State the blood parasite species.
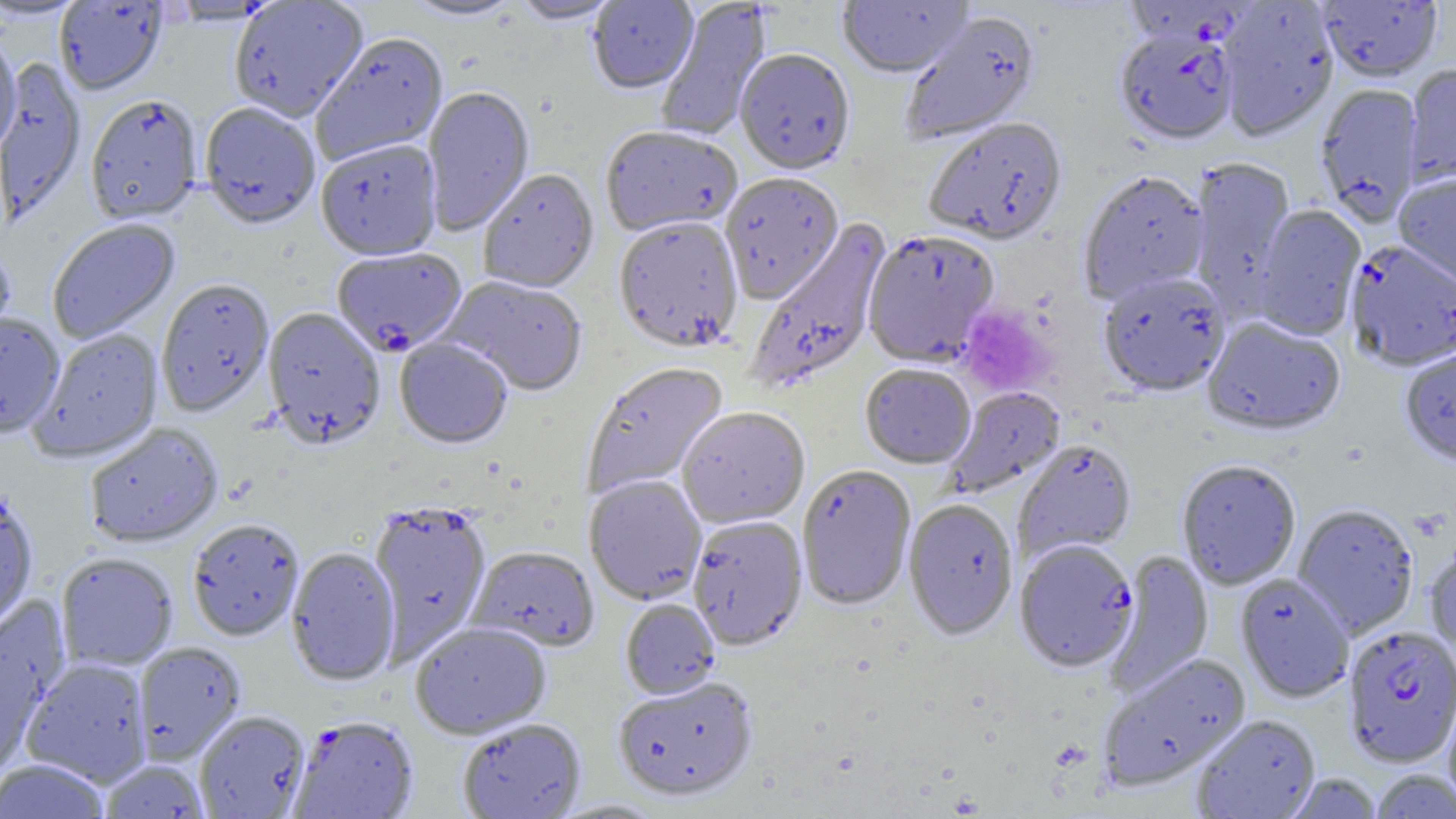

Plasmodium falciparum.

Summary:
  - Coordinate format: approximate bounding boxes as named x1/y1/x2/y2 corners in pixels
  - Platelet locations: (x1=957, y1=304, x2=1052, y2=396)
  - Plasmodium falciparum-infected red blood cell locations: (x1=1114, y1=30, x2=1237, y2=148), (x1=1345, y1=241, x2=1456, y2=373), (x1=332, y1=249, x2=467, y2=358), (x1=1015, y1=541, x2=1139, y2=675), (x1=1342, y1=627, x2=1455, y2=768), (x1=288, y1=716, x2=419, y2=818)
  - Uninfected red blood cell locations: (x1=400, y1=0, x2=524, y2=22), (x1=510, y1=0, x2=621, y2=25), (x1=655, y1=0, x2=772, y2=142), (x1=837, y1=0, x2=975, y2=81), (x1=1319, y1=0, x2=1443, y2=84), (x1=0, y1=1, x2=89, y2=20), (x1=587, y1=1, x2=699, y2=97), (x1=1217, y1=1, x2=1339, y2=143), (x1=55, y1=2, x2=168, y2=97), (x1=228, y1=2, x2=369, y2=123), (x1=900, y1=12, x2=1041, y2=146), (x1=0, y1=32, x2=21, y2=160), (x1=311, y1=34, x2=450, y2=165), (x1=735, y1=51, x2=856, y2=178), (x1=1, y1=60, x2=88, y2=229), (x1=1404, y1=65, x2=1456, y2=187), (x1=1314, y1=86, x2=1423, y2=226), (x1=421, y1=87, x2=535, y2=236), (x1=85, y1=97, x2=203, y2=227), (x1=199, y1=104, x2=321, y2=232), (x1=923, y1=119, x2=1068, y2=248), (x1=600, y1=127, x2=742, y2=238), (x1=315, y1=140, x2=443, y2=263), (x1=1187, y1=157, x2=1296, y2=316), (x1=478, y1=170, x2=599, y2=296), (x1=1079, y1=172, x2=1210, y2=304), (x1=720, y1=174, x2=844, y2=305), (x1=1394, y1=174, x2=1456, y2=289), (x1=1253, y1=204, x2=1367, y2=341), (x1=747, y1=217, x2=894, y2=393), (x1=48, y1=219, x2=181, y2=344), (x1=614, y1=219, x2=744, y2=354), (x1=862, y1=232, x2=999, y2=369), (x1=0, y1=245, x2=17, y2=352), (x1=1098, y1=275, x2=1230, y2=399), (x1=441, y1=276, x2=587, y2=398), (x1=156, y1=280, x2=274, y2=418), (x1=262, y1=308, x2=386, y2=451), (x1=0, y1=312, x2=65, y2=440), (x1=1202, y1=318, x2=1346, y2=438), (x1=29, y1=329, x2=165, y2=464), (x1=394, y1=339, x2=512, y2=451), (x1=1399, y1=349, x2=1456, y2=470), (x1=581, y1=363, x2=729, y2=498), (x1=860, y1=365, x2=976, y2=470), (x1=945, y1=387, x2=1066, y2=498), (x1=677, y1=408, x2=811, y2=530), (x1=84, y1=424, x2=224, y2=548), (x1=1013, y1=440, x2=1137, y2=564), (x1=1177, y1=461, x2=1301, y2=591), (x1=797, y1=467, x2=917, y2=612), (x1=584, y1=476, x2=707, y2=606), (x1=0, y1=492, x2=38, y2=637), (x1=903, y1=501, x2=1018, y2=642), (x1=367, y1=502, x2=492, y2=663), (x1=1293, y1=505, x2=1419, y2=639), (x1=687, y1=517, x2=808, y2=652), (x1=187, y1=520, x2=305, y2=642), (x1=1424, y1=544, x2=1456, y2=665), (x1=285, y1=548, x2=401, y2=687), (x1=467, y1=548, x2=599, y2=653), (x1=1106, y1=550, x2=1214, y2=698), (x1=56, y1=553, x2=178, y2=671), (x1=1235, y1=573, x2=1354, y2=704), (x1=0, y1=599, x2=71, y2=774), (x1=620, y1=599, x2=720, y2=700), (x1=410, y1=623, x2=551, y2=740), (x1=133, y1=642, x2=246, y2=765), (x1=1098, y1=654, x2=1252, y2=793), (x1=20, y1=658, x2=153, y2=788), (x1=613, y1=678, x2=759, y2=803), (x1=1443, y1=687, x2=1456, y2=813), (x1=193, y1=711, x2=311, y2=818), (x1=1191, y1=714, x2=1321, y2=819), (x1=457, y1=719, x2=587, y2=819), (x1=0, y1=760, x2=111, y2=819), (x1=100, y1=760, x2=209, y2=818), (x1=1370, y1=769, x2=1456, y2=819), (x1=1285, y1=773, x2=1384, y2=818)
  - Field of view: single
  - Modality: optical microscopy
  - Magnification: 1000x
  - Preparation: thin blood smear
  - Image size: 1456×819 pixels